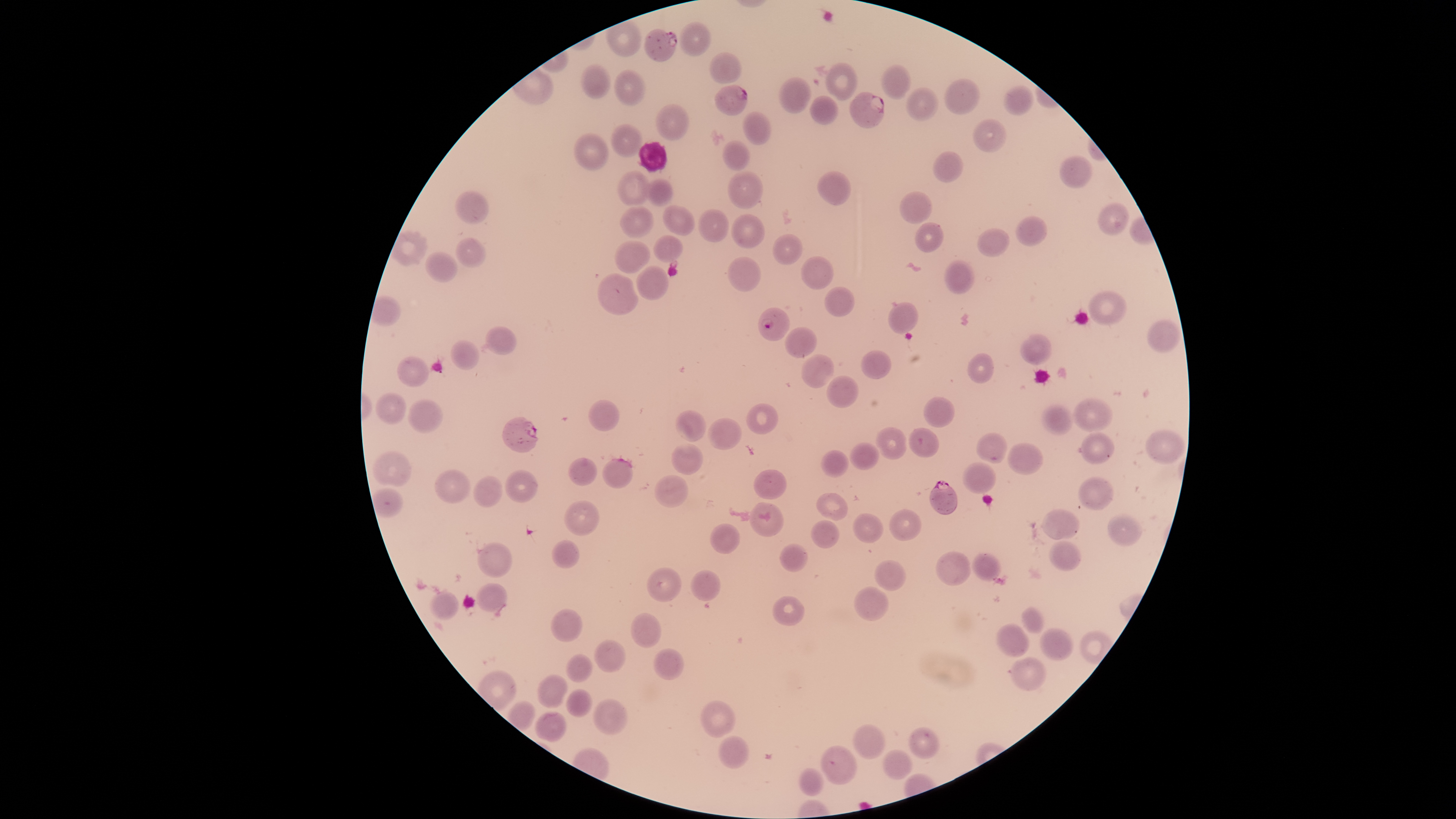
Approximate bounding boxes as [left, top, right, bottom] in pixels. Parasitized red blood cells: [646, 29, 677, 63], [715, 86, 749, 116], [851, 93, 885, 129], [758, 308, 790, 341], [502, 416, 538, 453], [929, 482, 958, 516]. Uninfected red blood cells: [679, 22, 711, 57], [709, 52, 742, 84], [824, 63, 858, 101], [580, 65, 610, 98], [880, 65, 912, 99], [614, 71, 645, 106], [778, 77, 810, 112], [945, 78, 980, 114], [1005, 85, 1033, 115], [905, 87, 939, 121], [809, 95, 839, 123], [654, 106, 688, 140], [743, 112, 771, 145], [974, 119, 1007, 152], [610, 123, 641, 159], [573, 133, 607, 172], [722, 140, 750, 169], [933, 152, 963, 184], [1059, 156, 1093, 189], [818, 170, 851, 204], [728, 171, 763, 210], [619, 172, 648, 205], [646, 180, 673, 206], [454, 191, 490, 225], [900, 192, 931, 223], [1098, 202, 1130, 236], [664, 205, 695, 236], [621, 207, 655, 237], [699, 210, 730, 242], [732, 214, 765, 247], [1017, 216, 1046, 247], [916, 223, 945, 252], [977, 229, 1012, 257], [772, 233, 802, 265], [654, 236, 683, 262], [455, 238, 485, 268], [616, 241, 650, 274], [425, 252, 459, 282], [802, 256, 833, 290], [727, 258, 762, 291], [945, 260, 972, 295], [637, 266, 669, 300], [598, 274, 640, 316], [824, 288, 855, 317], [1089, 290, 1127, 326], [888, 303, 918, 334], [1147, 320, 1180, 353], [485, 327, 517, 356], [785, 328, 818, 358], [1021, 333, 1053, 366], [450, 341, 480, 371], [861, 350, 891, 379], [800, 353, 835, 389], [967, 354, 996, 383], [396, 356, 428, 388], [827, 376, 859, 409], [375, 393, 407, 425], [924, 396, 955, 429], [1073, 399, 1114, 432], [407, 400, 444, 434], [589, 401, 621, 432], [746, 404, 779, 435], [1041, 404, 1073, 434], [675, 410, 706, 443], [707, 418, 742, 450], [874, 427, 909, 458], [908, 427, 940, 459], [1145, 428, 1186, 464], [977, 433, 1006, 463], [1080, 433, 1115, 464], [849, 441, 876, 471], [670, 442, 704, 474], [1006, 443, 1044, 475], [822, 449, 849, 479], [371, 452, 413, 487], [569, 456, 597, 487], [602, 458, 634, 489], [964, 463, 995, 495], [505, 469, 538, 503], [753, 469, 787, 501], [435, 470, 471, 504], [655, 475, 688, 508], [473, 476, 504, 508], [1077, 477, 1114, 510], [816, 493, 849, 520], [565, 502, 599, 536], [749, 502, 783, 537], [889, 508, 921, 542], [1043, 510, 1080, 541], [853, 514, 883, 544], [1108, 514, 1142, 547], [811, 519, 839, 550], [709, 525, 740, 554], [1050, 540, 1080, 573], [553, 542, 580, 569], [478, 543, 513, 578], [780, 544, 807, 573], [937, 552, 970, 587], [973, 552, 1002, 582], [875, 560, 906, 591], [648, 568, 682, 602], [690, 569, 720, 603], [476, 584, 508, 611], [854, 587, 888, 621], [429, 592, 458, 620], [774, 597, 804, 626], [1022, 608, 1044, 634], [552, 609, 583, 642], [632, 612, 662, 649], [996, 623, 1029, 658], [1041, 628, 1073, 662], [594, 640, 625, 672], [653, 648, 684, 680], [568, 654, 593, 681], [1010, 657, 1046, 692], [536, 675, 569, 709], [566, 689, 592, 719], [593, 699, 628, 735], [701, 702, 735, 737], [534, 712, 567, 742], [852, 725, 885, 760], [909, 727, 939, 760], [718, 735, 750, 769], [821, 747, 855, 786], [884, 749, 911, 781], [800, 767, 823, 796]. Smartphone photograph through the microscope eyepiece. Species: Plasmodium falciparum. Presence: malaria parasites seen. Giemsa-stained preparation. Single field of view. Thin smear of blood. Image is 1456×819 pixels. Circular visible region.